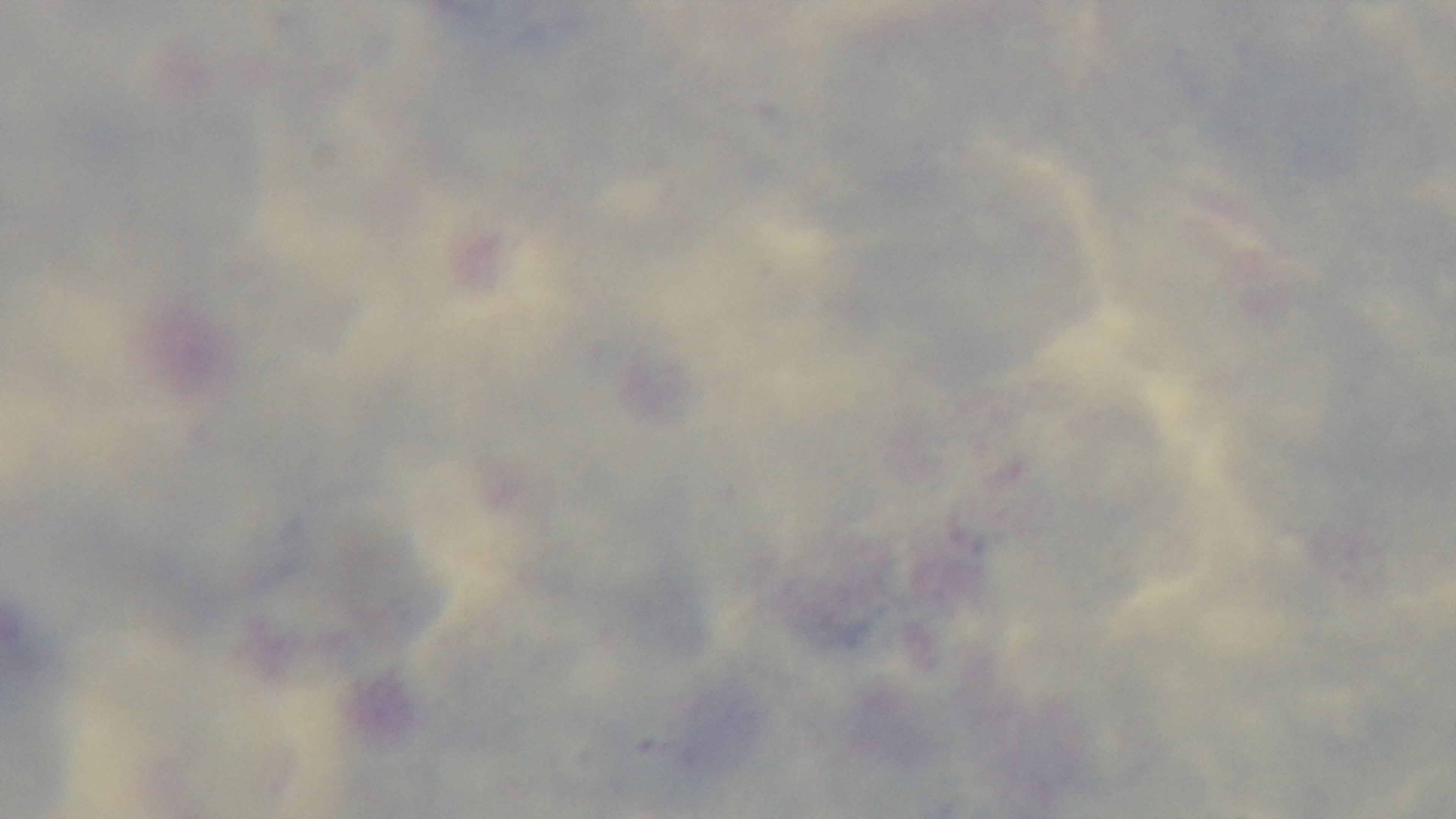

Summary:
  - Objective: 100x oil immersion
  - Capture: mounted 4K digital camera
  - Stain: Giemsa
  - Field of view: one from the slide
  - Malaria status: negative
  - Preparation: thick
  - Modality: light microscopy